Report the malaria status of this cell.
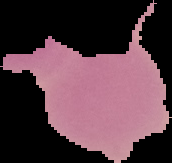

It is uninfected.

{
  "image_size": "172×163 pixels",
  "image_type": "segmented cell region with the area outside set to black",
  "preparation": "thin blood film"
}